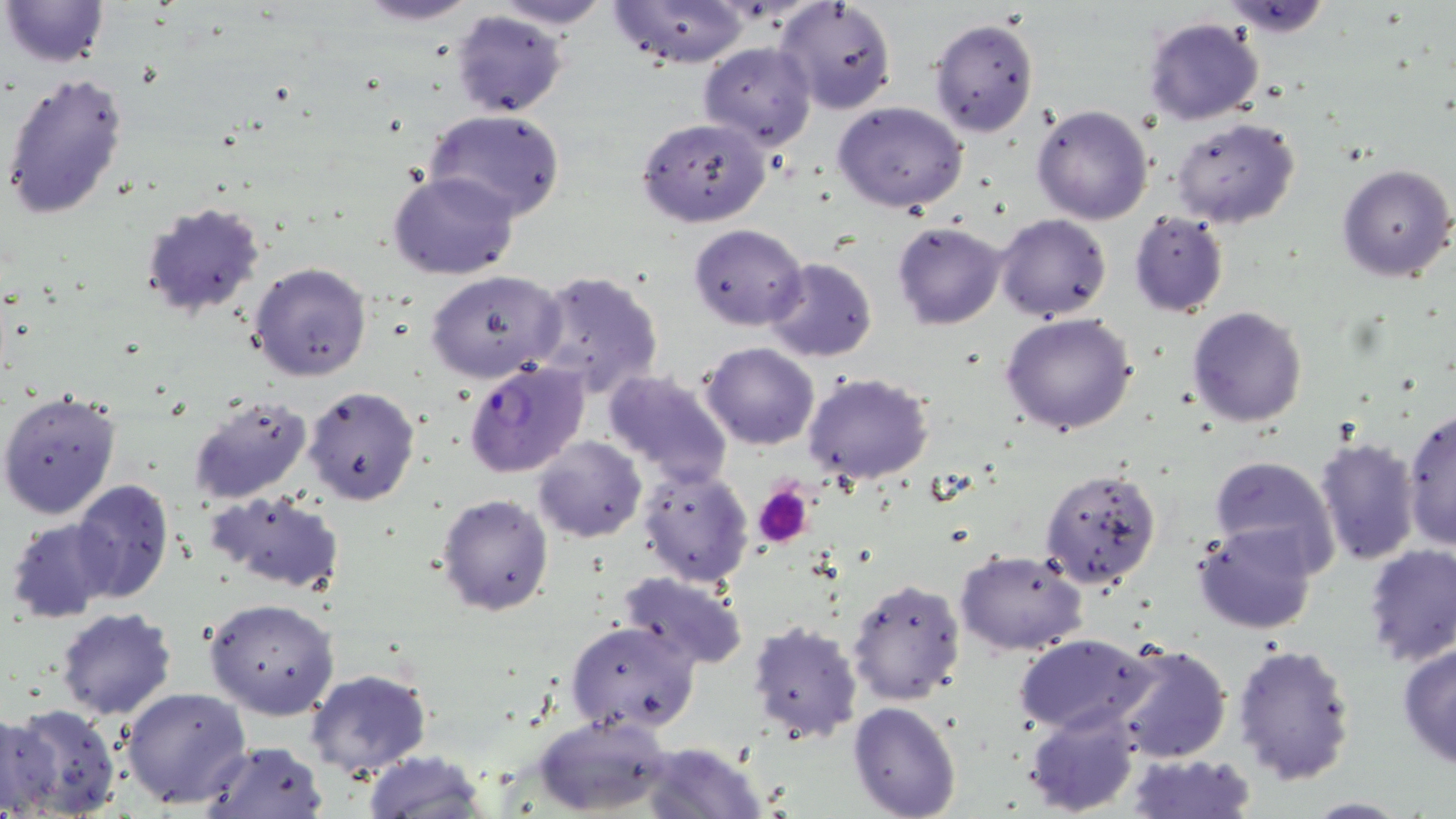
Summary:
  - Coordinate format: approximate bounding boxes as named x1/y1/x2/y2 corners in pixels
  - Platelet locations: (x1=755, y1=484, x2=813, y2=547)
  - Uninfected red blood cell locations: (x1=2, y1=0, x2=108, y2=70), (x1=352, y1=0, x2=483, y2=25), (x1=490, y1=0, x2=612, y2=31), (x1=611, y1=1, x2=748, y2=68), (x1=777, y1=1, x2=897, y2=115), (x1=1218, y1=1, x2=1336, y2=35), (x1=450, y1=10, x2=569, y2=119), (x1=1142, y1=16, x2=1265, y2=127), (x1=929, y1=17, x2=1039, y2=138), (x1=698, y1=41, x2=816, y2=149), (x1=1, y1=70, x2=131, y2=220), (x1=832, y1=101, x2=970, y2=215), (x1=1030, y1=104, x2=1154, y2=225), (x1=425, y1=109, x2=566, y2=223), (x1=637, y1=116, x2=770, y2=227), (x1=1170, y1=117, x2=1301, y2=228), (x1=1336, y1=163, x2=1454, y2=282), (x1=387, y1=170, x2=520, y2=280), (x1=141, y1=203, x2=268, y2=320), (x1=1128, y1=212, x2=1230, y2=316), (x1=995, y1=213, x2=1111, y2=322), (x1=892, y1=221, x2=1008, y2=331), (x1=688, y1=223, x2=809, y2=331), (x1=764, y1=258, x2=878, y2=362), (x1=248, y1=261, x2=374, y2=384), (x1=424, y1=269, x2=566, y2=384), (x1=532, y1=271, x2=665, y2=399), (x1=1187, y1=306, x2=1308, y2=427), (x1=999, y1=313, x2=1138, y2=436), (x1=700, y1=342, x2=821, y2=450), (x1=602, y1=368, x2=734, y2=486), (x1=802, y1=372, x2=934, y2=485), (x1=303, y1=386, x2=421, y2=505), (x1=0, y1=390, x2=122, y2=521), (x1=186, y1=395, x2=314, y2=505), (x1=1402, y1=405, x2=1456, y2=551), (x1=533, y1=436, x2=646, y2=544), (x1=1314, y1=436, x2=1421, y2=566), (x1=1208, y1=454, x2=1341, y2=575), (x1=639, y1=464, x2=754, y2=586), (x1=1039, y1=466, x2=1162, y2=590), (x1=69, y1=479, x2=174, y2=603), (x1=208, y1=489, x2=347, y2=594), (x1=435, y1=493, x2=554, y2=616), (x1=6, y1=517, x2=120, y2=623), (x1=1194, y1=522, x2=1318, y2=635), (x1=1362, y1=543, x2=1455, y2=666), (x1=955, y1=548, x2=1088, y2=656), (x1=619, y1=570, x2=750, y2=670), (x1=845, y1=575, x2=966, y2=707), (x1=204, y1=598, x2=341, y2=719), (x1=55, y1=607, x2=178, y2=721), (x1=748, y1=616, x2=864, y2=744), (x1=566, y1=620, x2=701, y2=735), (x1=1015, y1=631, x2=1158, y2=737), (x1=1232, y1=641, x2=1358, y2=785), (x1=1110, y1=643, x2=1232, y2=764), (x1=1397, y1=643, x2=1456, y2=770), (x1=305, y1=669, x2=433, y2=781), (x1=121, y1=685, x2=251, y2=809), (x1=848, y1=701, x2=962, y2=819), (x1=4, y1=703, x2=121, y2=818), (x1=1025, y1=708, x2=1141, y2=816), (x1=0, y1=712, x2=58, y2=816), (x1=533, y1=714, x2=674, y2=816), (x1=200, y1=740, x2=328, y2=819), (x1=643, y1=741, x2=766, y2=819), (x1=361, y1=750, x2=488, y2=818), (x1=1127, y1=751, x2=1253, y2=818), (x1=1301, y1=797, x2=1414, y2=817)
  - Plasmodium falciparum-infected red blood cell locations: (x1=463, y1=360, x2=589, y2=479)
  - Slide-level diagnosis: Plasmodium falciparum
  - Image size: 1456×819 pixels
  - Modality: optical microscopy
  - Field of view: one of a larger specimen
  - Preparation: thin blood smear
  - Stain: May-Grünwald-Giemsa
  - Magnification: 1000x